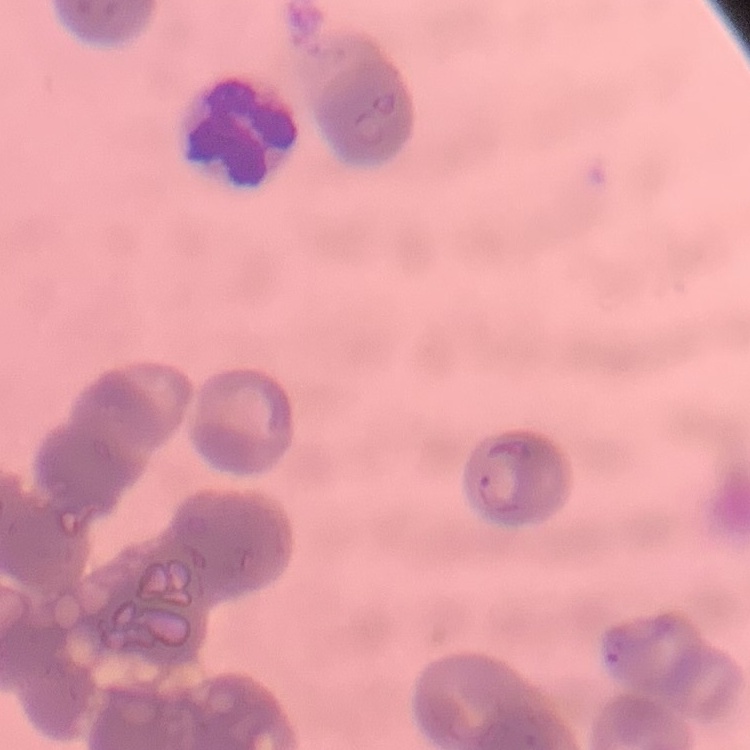
erythrocyte morphology = rouleaux formation
stain = Field's or Giemsa
preparation = thin blood film
image type = one tile cut from a larger photomicrograph